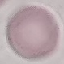

Summary:
  - Malaria status: uninfected
  - Preparation: thin blood film
  - Image type: cell patch, automatically extracted from a larger field of view and resized to 64 × 64 pixels
  - Stain: Giemsa
  - Capture: smartphone through the microscope eyepiece